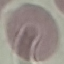 Malaria status: uninfected. Cell patch, automatically extracted from a larger field of view and resized to 64 × 64 pixels. Thin blood film. Giemsa-stained preparation. Acquired by smartphone through the microscope eyepiece.